Name the parasite shown.
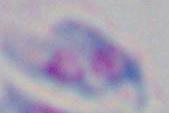

This is Toxoplasma gondii.

Summary:
  - Modality: micrograph
  - Magnification: 1000x